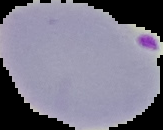
result = Plasmodium parasites identified
image type = segmented cell region with the area outside set to black
preparation = thin blood film
image size = 163×130 pixels